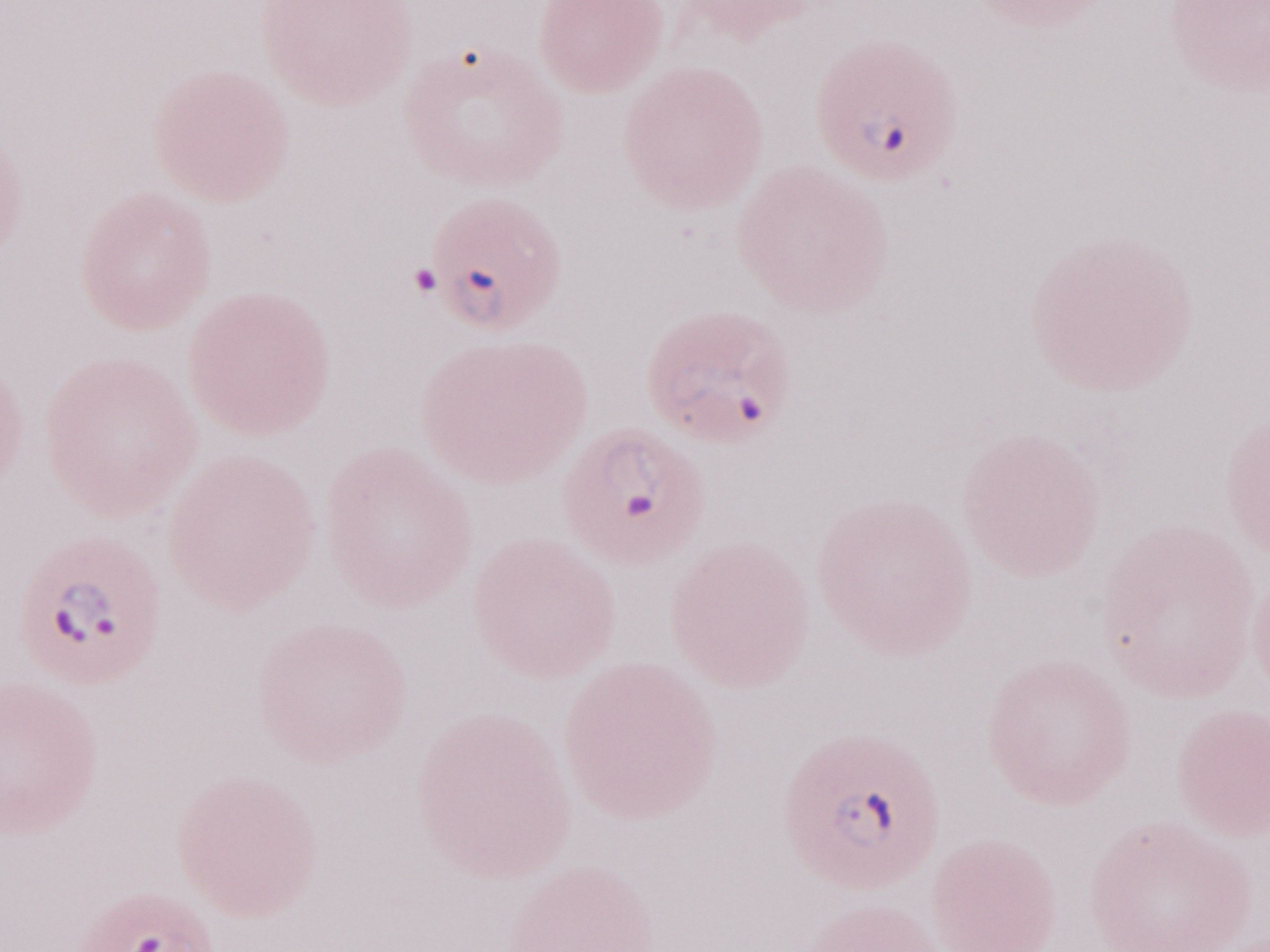

Image is 1270×952 pixels. Thin peripheral-blood smear. One field of this slide. Olympus BX43 microscope, Olympus DP73 camera. Patient-level malaria diagnosis: positive. 1,000x magnification. May-Grünwald-Giemsa stain.